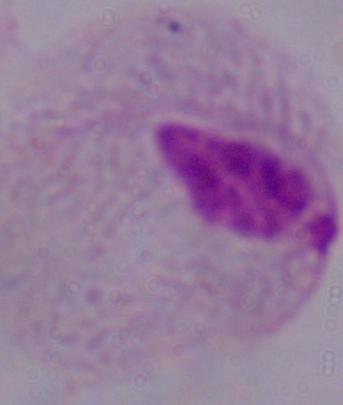
modality = micrograph
identification = trichomonad
magnification = 1000x